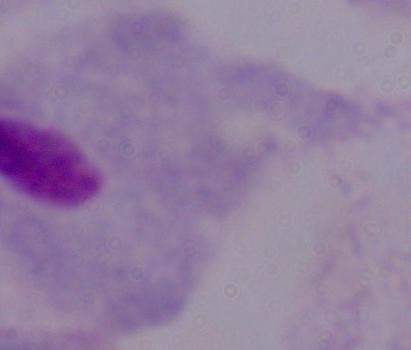
{
  "magnification": "1000x",
  "modality": "micrograph",
  "identification": "trichomonad"
}